Identify the cell.
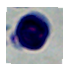
This is a leukocyte.

Photomicrograph. Captured at 1000x magnification.